Assess this cell for malaria.
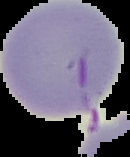
Uninfected.

From a thin blood smear. The area outside the segmented cell region is set to black. Image is 130×157 pixels.